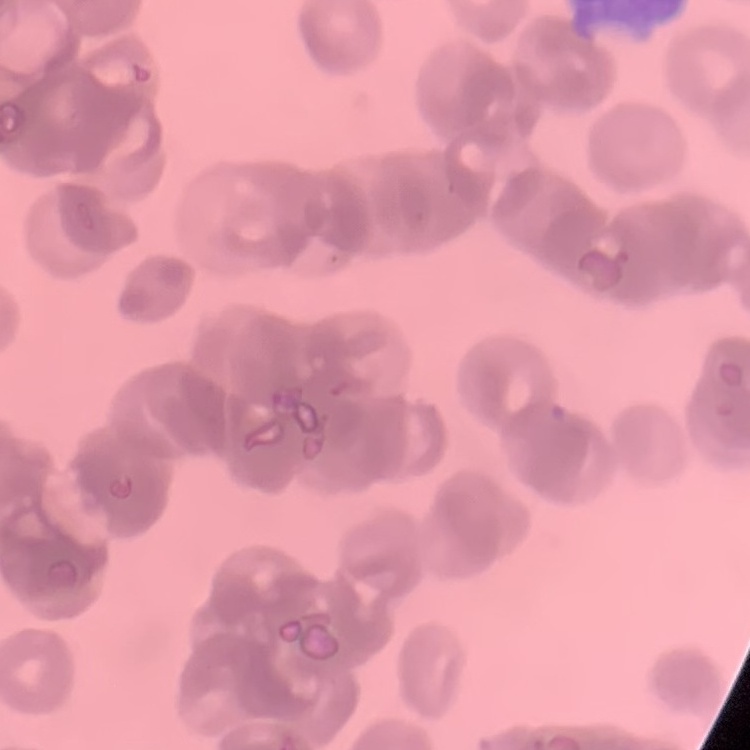

{
  "erythrocyte_morphology": "rouleaux formation",
  "preparation": "thin peripheral smear",
  "image_type": "one tile cut from a larger photomicrograph",
  "stain": "Field's or Giemsa"
}